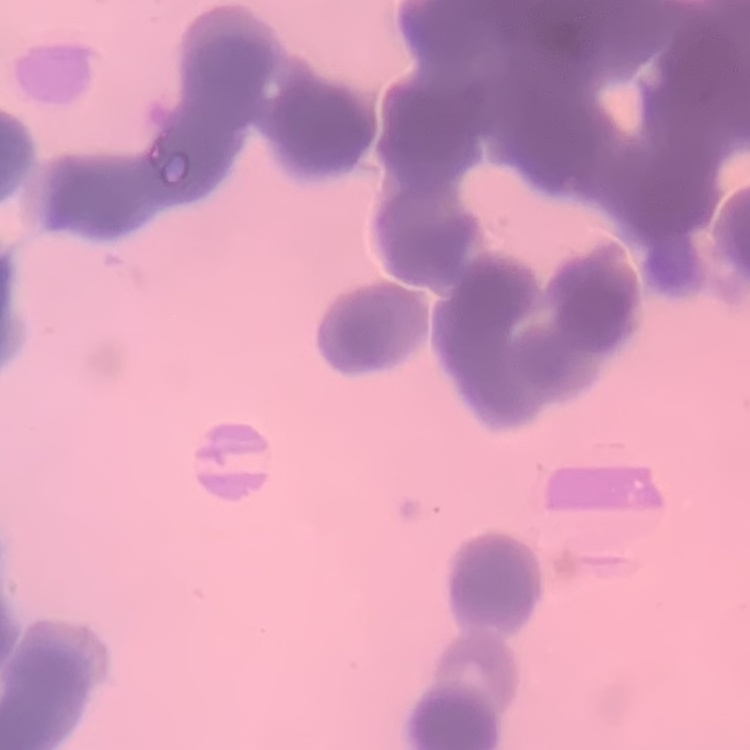
Summary:
  - Red blood cell morphology: rouleaux formation
  - Preparation: thin peripheral smear
  - Stain: Field's or Giemsa
  - Image type: one tile cut from a larger photomicrograph